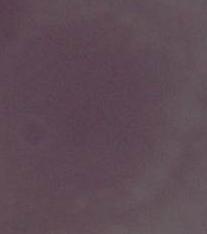

{
  "identification": "red blood cell",
  "modality": "micrograph",
  "magnification": "1000x"
}